Identify the cell.
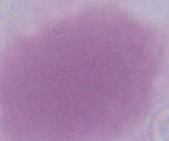

An erythrocyte.

1000x magnification. Photomicrograph.